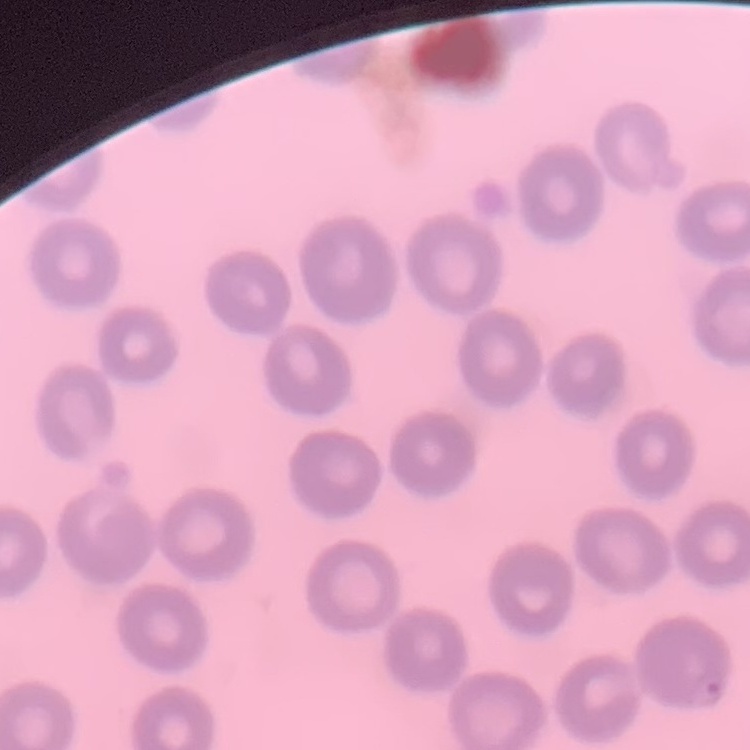
erythrocyte morphology = no rouleaux formation
stain = Field's or Giemsa
preparation = thin blood smear
image type = one tile cut from a larger photomicrograph